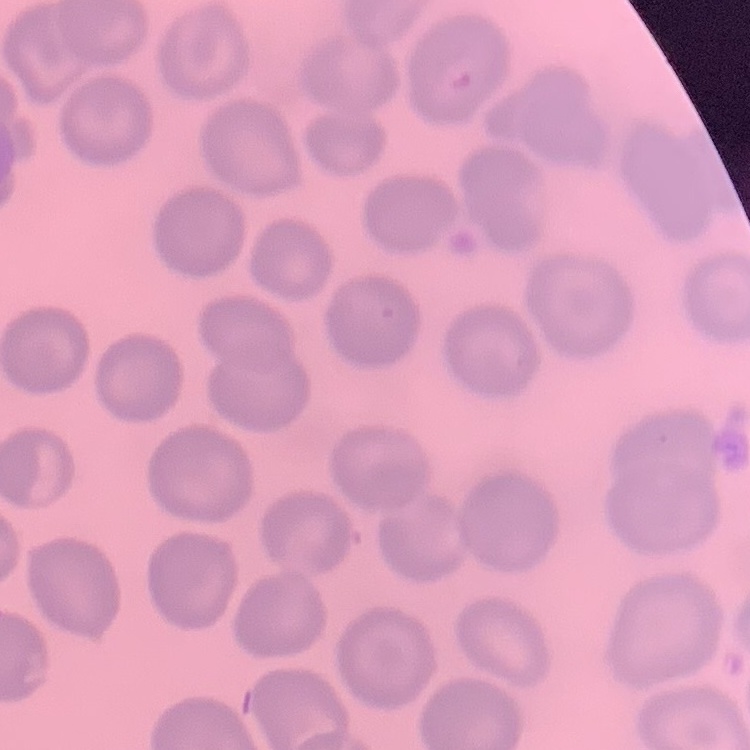

Summary:
  - Red blood cell morphology: no rouleaux formation
  - Image type: square crop of a larger photomicrograph
  - Stain: Field's or Giemsa
  - Preparation: thin blood film